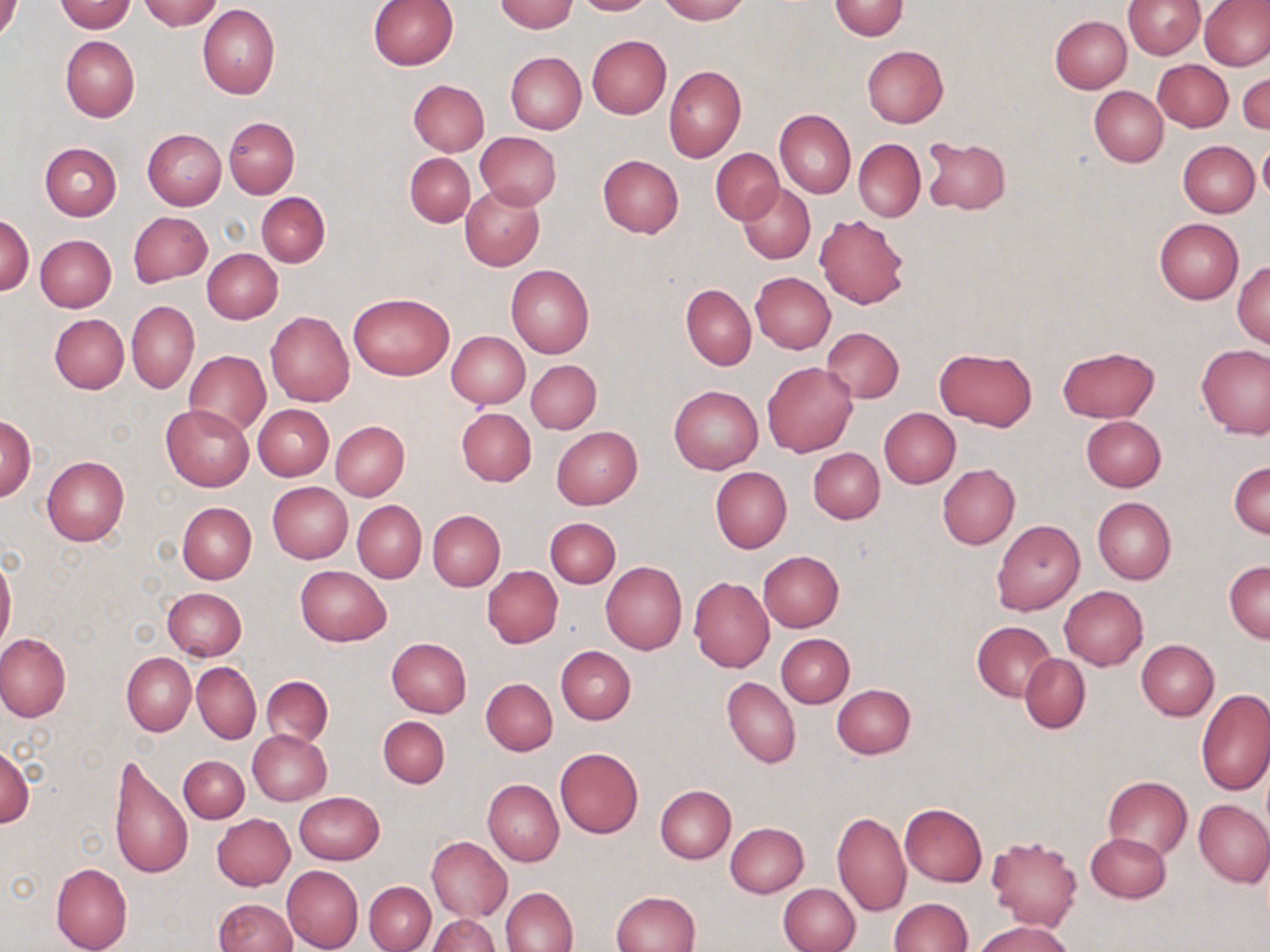
Approximate bounding boxes as (x1,y1)-(x2,y2) corner pairs in pixels. Uninfected red blood cell locations: (0,0)-(23,42), (57,0)-(134,33), (138,0)-(224,30), (572,0)-(653,15), (658,0)-(748,23), (1122,0)-(1204,59), (368,1)-(457,71), (495,1)-(578,32), (829,1)-(908,39), (1198,1)-(1270,70), (198,4)-(280,99), (1050,16)-(1132,92), (587,35)-(671,119), (61,36)-(140,121), (861,46)-(949,128), (505,51)-(586,134), (1154,59)-(1233,131), (664,66)-(746,162), (1238,70)-(1270,136), (407,79)-(489,156), (1090,86)-(1168,166), (775,110)-(855,198), (224,118)-(299,197), (143,129)-(226,209), (474,132)-(562,209), (923,136)-(1012,215), (854,139)-(925,221), (1258,140)-(1270,205), (1178,141)-(1258,217), (40,143)-(121,220), (712,148)-(783,223), (405,153)-(474,226), (597,154)-(684,238), (738,182)-(815,263), (461,185)-(545,270), (256,192)-(330,268), (128,212)-(211,285), (0,214)-(33,295), (815,214)-(908,309), (1154,218)-(1244,303), (35,234)-(116,312), (203,248)-(282,323), (1233,261)-(1270,348), (506,264)-(594,358), (750,272)-(836,353), (681,284)-(757,370), (347,293)-(454,381), (127,302)-(198,392), (265,310)-(355,407), (50,314)-(129,393), (257,314)-(341,482), (821,327)-(903,403), (446,331)-(530,408), (1196,343)-(1270,438), (1057,345)-(1160,422), (934,348)-(1038,430), (183,350)-(270,438), (526,360)-(601,434), (762,362)-(857,457), (669,385)-(762,473), (253,404)-(333,480), (160,405)-(254,491), (456,407)-(536,485), (880,408)-(960,488), (1,414)-(36,502), (1081,416)-(1166,492), (331,421)-(409,501), (551,426)-(643,508), (808,448)-(885,524), (41,456)-(129,547), (1229,462)-(1269,539), (937,464)-(1019,549), (711,466)-(791,553), (267,481)-(353,564), (1092,497)-(1175,586), (353,500)-(426,583), (178,503)-(256,583), (427,510)-(505,591), (545,517)-(620,588), (992,519)-(1084,616), (757,550)-(843,632), (0,553)-(16,654), (1224,560)-(1270,643), (600,561)-(687,655), (295,565)-(391,646), (482,566)-(562,647), (689,576)-(774,672), (1059,586)-(1148,669), (162,587)-(247,660), (972,622)-(1057,701), (0,633)-(71,722), (776,633)-(854,708), (386,637)-(472,717), (1137,640)-(1218,719), (556,646)-(635,724), (122,653)-(195,735), (1020,655)-(1090,733), (193,662)-(261,743), (261,676)-(333,746), (722,677)-(800,768), (481,678)-(557,755), (832,684)-(916,759), (1196,689)-(1270,794), (378,715)-(450,788), (248,729)-(331,805), (0,744)-(34,828), (555,747)-(644,839), (108,753)-(193,882), (178,755)-(249,823), (1103,777)-(1192,859), (482,779)-(563,865), (655,785)-(735,863), (294,792)-(384,865), (1195,801)-(1270,886), (899,803)-(987,887), (831,809)-(910,916), (212,814)-(295,890), (725,822)-(808,898), (1086,832)-(1171,902), (985,835)-(1083,930), (426,836)-(512,922), (51,863)-(132,952), (282,865)-(363,951), (363,881)-(436,952), (778,883)-(859,952), (501,887)-(578,951), (612,890)-(701,952), (214,898)-(297,952), (888,899)-(972,951), (428,915)-(501,951), (973,920)-(1077,952). Slide-level diagnosis: negative for blood parasites. May-Grünwald-Giemsa-stained preparation. Light microscopy. Thin blood smear. Image is 1270×952 pixels. 1000x magnification. One field of a larger specimen.